Locate every blood parasite and identify its species.
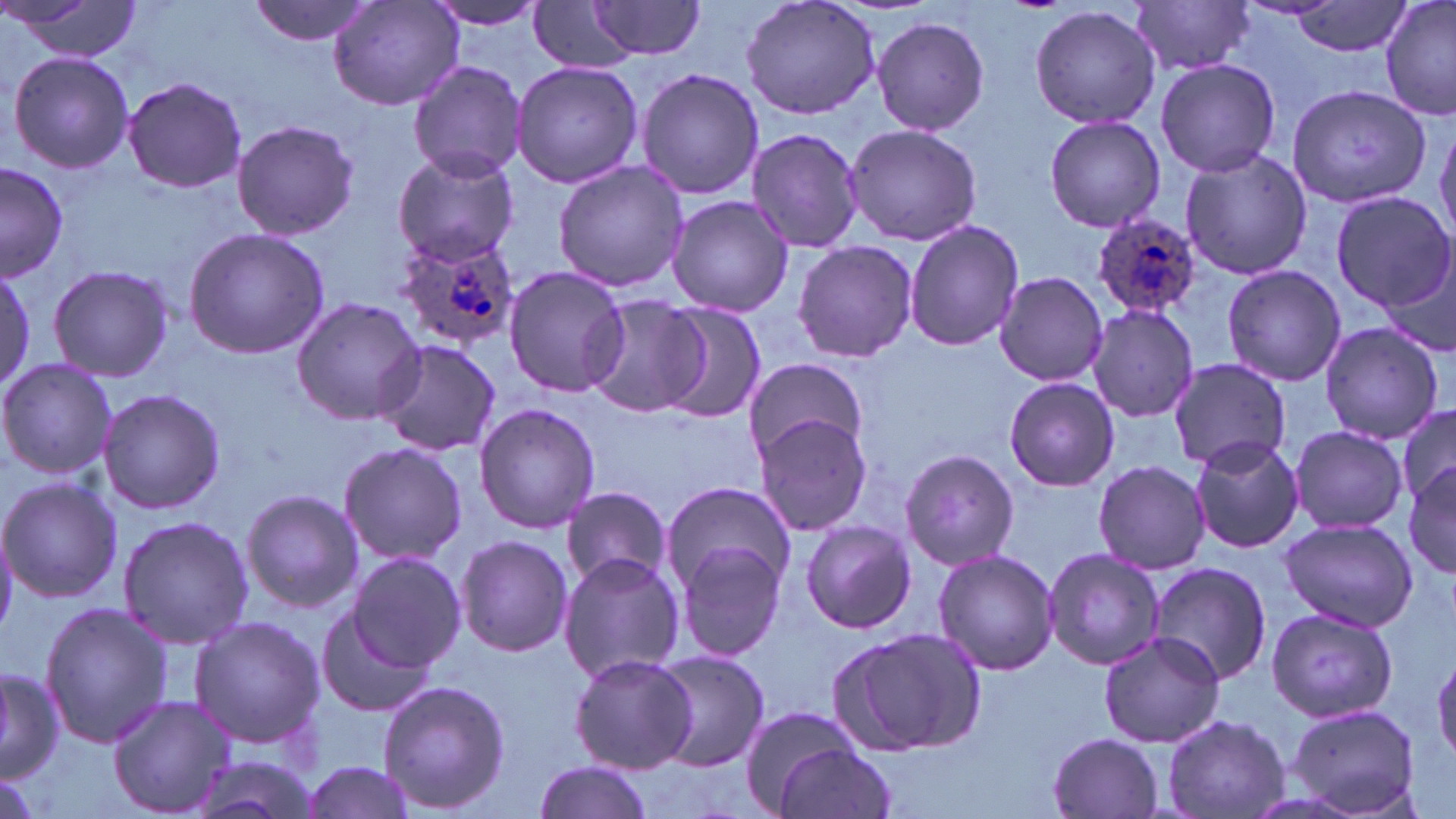

Approximate bounding boxes as (x1, y1, x2, y2) in pixels.
Plasmodium ovale-infected red blood cells: (1094, 213, 1204, 321), (391, 233, 521, 350).
No Plasmodium falciparum, Plasmodium malariae, Plasmodium vivax, Babesia divergens, or Trypanosoma brucei observed.

slide-level diagnosis = Plasmodium ovale
uninfected red blood cell locations = approximate bounding boxes as (x1, y1, x2, y2) in pixels: (247, 0, 378, 46), (739, 0, 883, 120), (1380, 0, 1456, 122), (5, 1, 144, 62), (329, 1, 463, 112), (423, 1, 550, 31), (584, 1, 709, 61), (1131, 1, 1256, 77), (1289, 1, 1413, 58), (528, 3, 637, 74), (1029, 5, 1162, 131), (871, 14, 990, 135), (6, 51, 134, 172), (1156, 59, 1281, 178), (408, 60, 527, 181), (509, 61, 643, 190), (635, 68, 765, 201), (122, 76, 247, 194), (1287, 83, 1432, 208), (1042, 115, 1166, 233), (1435, 117, 1456, 245), (230, 119, 359, 241), (843, 123, 983, 245), (745, 126, 866, 254), (392, 147, 519, 267), (1178, 148, 1313, 281), (0, 161, 69, 280), (553, 161, 690, 293), (1329, 190, 1455, 311), (665, 195, 794, 317), (905, 219, 1024, 352), (183, 228, 332, 359), (793, 239, 917, 362), (1379, 254, 1455, 361), (0, 259, 36, 392), (48, 264, 173, 383), (1222, 264, 1346, 387), (503, 267, 629, 399), (992, 271, 1108, 387), (290, 296, 424, 425), (580, 296, 707, 418), (654, 302, 766, 422), (1086, 305, 1200, 424), (1318, 322, 1445, 444), (371, 340, 502, 458), (0, 357, 116, 482), (1168, 357, 1291, 470), (742, 359, 868, 458), (1003, 377, 1119, 492), (97, 387, 226, 516), (473, 402, 600, 534), (1394, 403, 1456, 513), (750, 411, 875, 536), (1288, 425, 1408, 534), (1189, 434, 1305, 554), (338, 441, 470, 568), (899, 447, 1020, 571), (1093, 461, 1208, 573), (1404, 463, 1456, 578), (0, 476, 121, 604), (661, 480, 797, 594), (560, 487, 672, 592), (238, 488, 363, 613), (118, 515, 255, 649), (1278, 517, 1420, 633), (799, 519, 916, 635), (455, 534, 574, 658), (674, 541, 788, 663), (1040, 546, 1166, 672), (932, 549, 1061, 677), (347, 551, 467, 672), (559, 555, 686, 683), (1146, 562, 1272, 687), (39, 600, 171, 748), (315, 604, 440, 720), (1266, 608, 1397, 722), (189, 615, 327, 749), (828, 624, 987, 757), (1097, 632, 1225, 748), (650, 650, 770, 770), (568, 653, 696, 773), (0, 664, 63, 783), (376, 679, 511, 815), (108, 695, 234, 816), (1285, 702, 1422, 818), (735, 704, 865, 814), (1162, 713, 1289, 818), (1045, 732, 1166, 818), (770, 740, 899, 819), (185, 755, 324, 819), (297, 758, 421, 819), (533, 758, 656, 819)
magnification = 1000x
image size = 1456×819 pixels
stain = May-Grünwald-Giemsa
field of view = single
modality = optical microscopy
preparation = thin blood film